Report the malaria status of this cell.
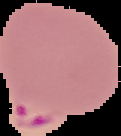
It is parasitized.

From a thin blood film. Image is 121×136 pixels. Cell region segmented out of the field of view; the surrounding area is masked to black.